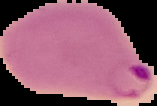
preparation = thin blood smear
image size = 157×106 pixels
malaria status = parasitized
image type = cell region segmented out of the field of view; surrounding area masked to black